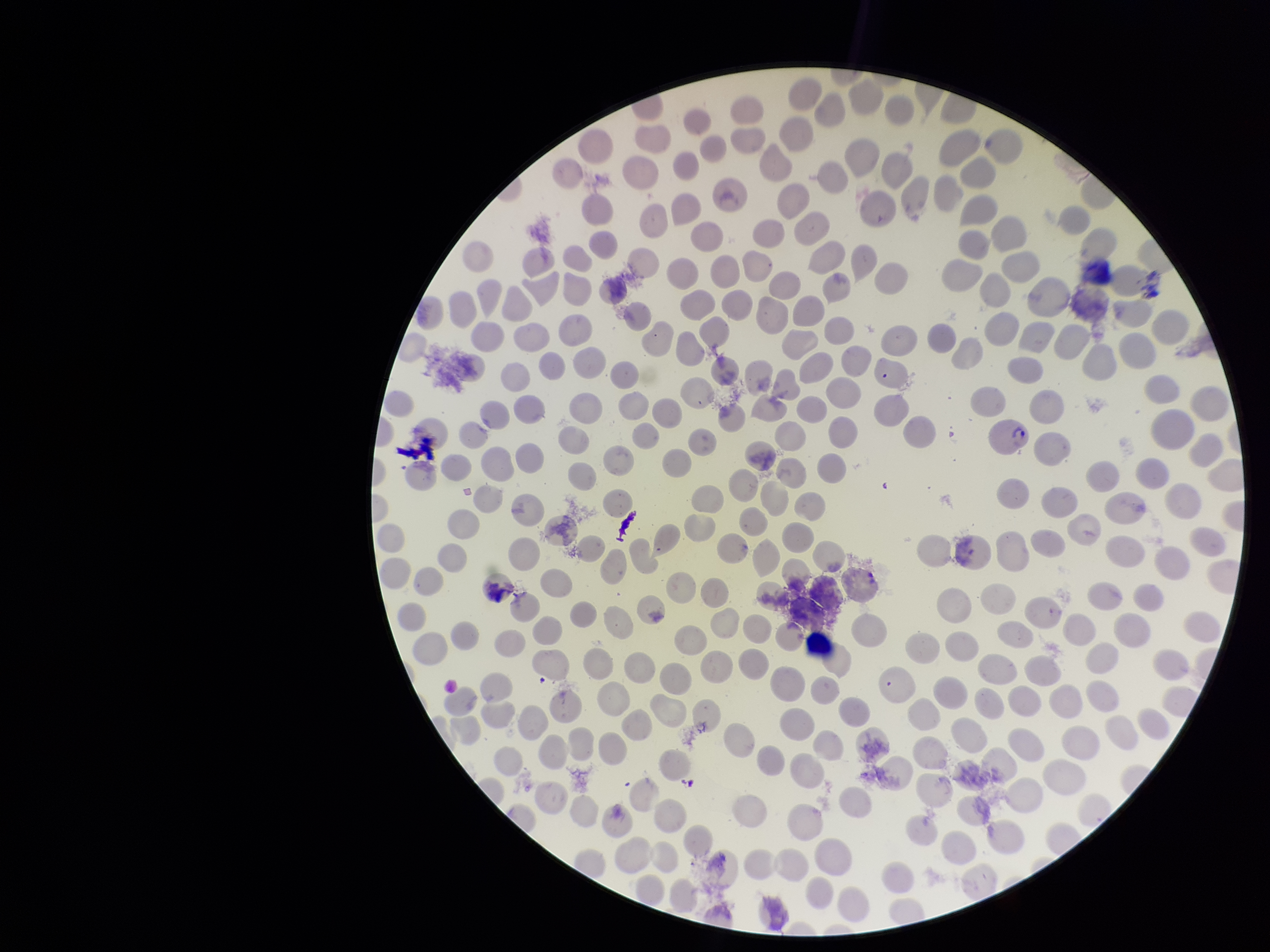
Patient malaria status: infected. Parasitized red blood cells: detected. Preparation: thin. Single field of view. Smartphone photograph taken through the eyepiece of a microscope. Image is 1270×952 pixels. Giemsa stain. Parasitized red blood cell count: 1. Species reported for this patient: Plasmodium vivax. Red blood cell count: 201.